Comment on the morphology of the red blood cells.
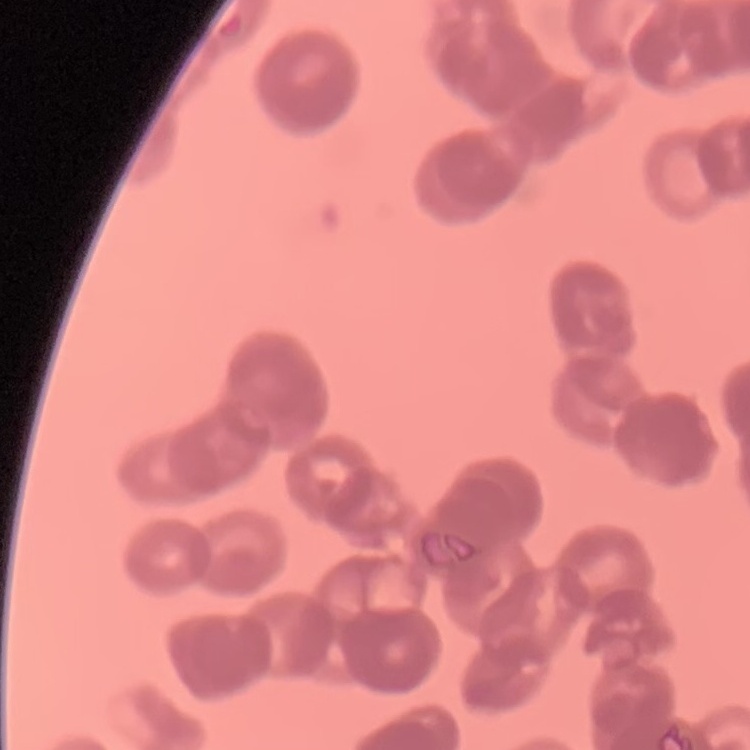
They show rouleaux formation.

image_type: one tile cut from a larger photomicrograph
preparation: thin peripheral smear
stain: Field's or Giemsa